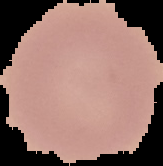
image_type: cell region segmented out of the field of view; surrounding area masked to black
result: no malaria parasites detected
image_size: 163×166 pixels
preparation: thin blood smear